Assess the morphology of the red blood cells.
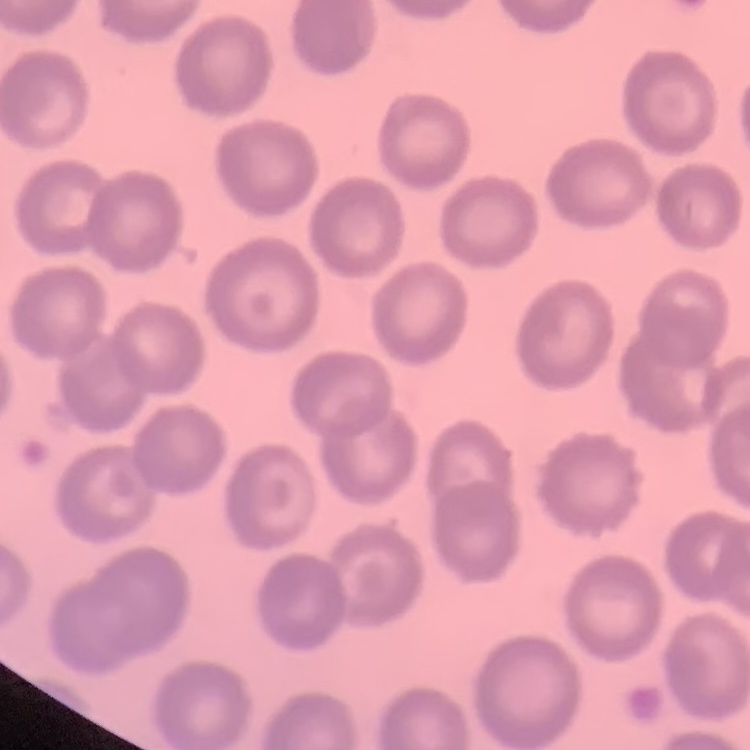
No rouleaux formation.

Summary:
  - Stain: Field's or Giemsa
  - Preparation: thin blood film
  - Image type: one tile cut from a larger photomicrograph